Point out malaria parasites and leukocytes.
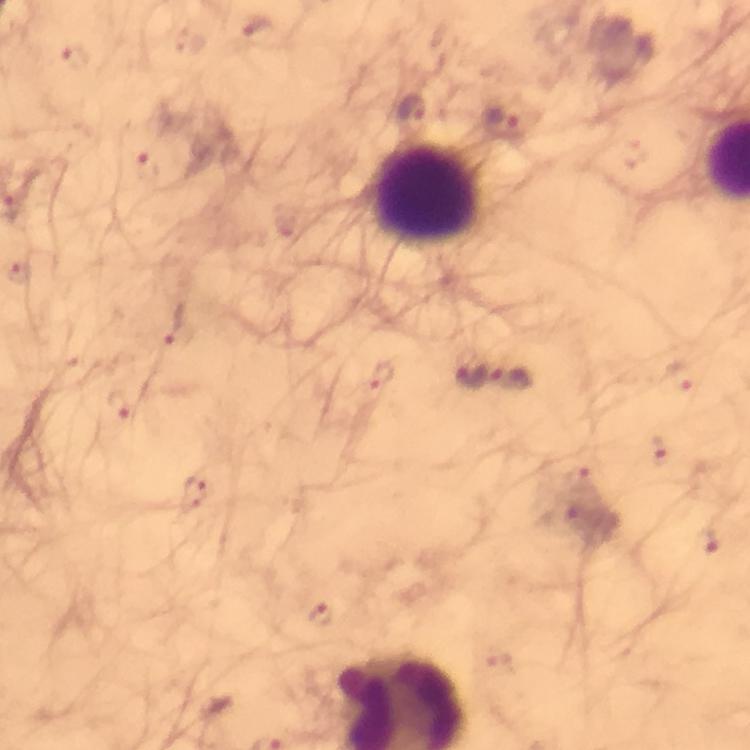
Approximate object centers, in pixels from the top-left corner.
Malaria parasites: (x=260, y=30), (x=74, y=56), (x=415, y=110), (x=505, y=125), (x=148, y=166), (x=19, y=273), (x=176, y=325), (x=470, y=376), (x=382, y=377), (x=513, y=379), (x=682, y=380), (x=116, y=405), (x=655, y=450), (x=582, y=477), (x=196, y=494), (x=562, y=518), (x=708, y=545), (x=320, y=615), (x=498, y=662).
Leukocytes: (x=430, y=195).

{
  "magnification": "100x",
  "capture": "smartphone camera through the microscope",
  "context": "from a malaria diagnostic workup",
  "stain": "Giemsa",
  "immersion_oil": "used",
  "preparation": "thick blood smear",
  "cropped_from": "a single field of view",
  "image_size": "750×750 pixels"
}